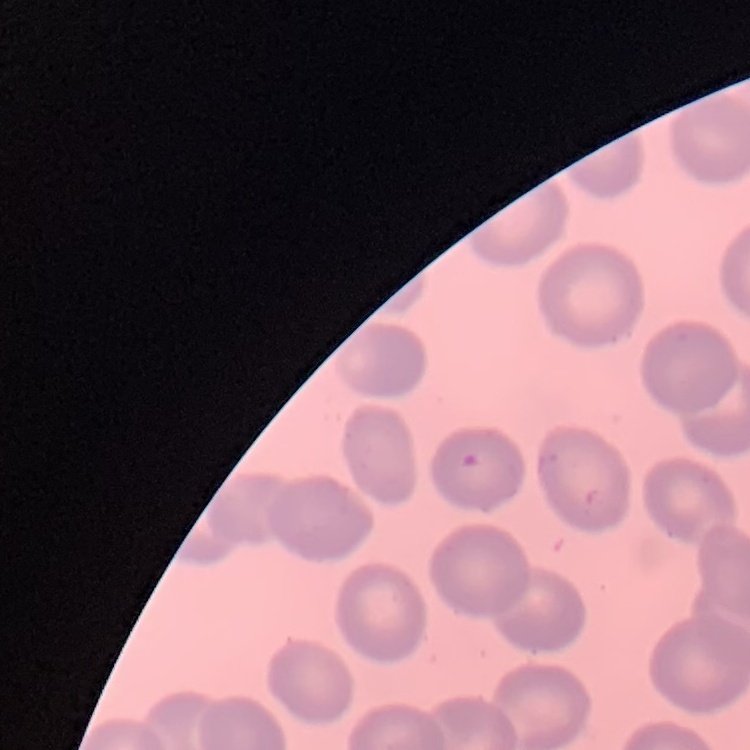

The red blood cells exhibit no rouleaux formation. One tile cut from a larger photomicrograph. Field's or Giemsa stain. Thin blood film.